Assess for malaria.
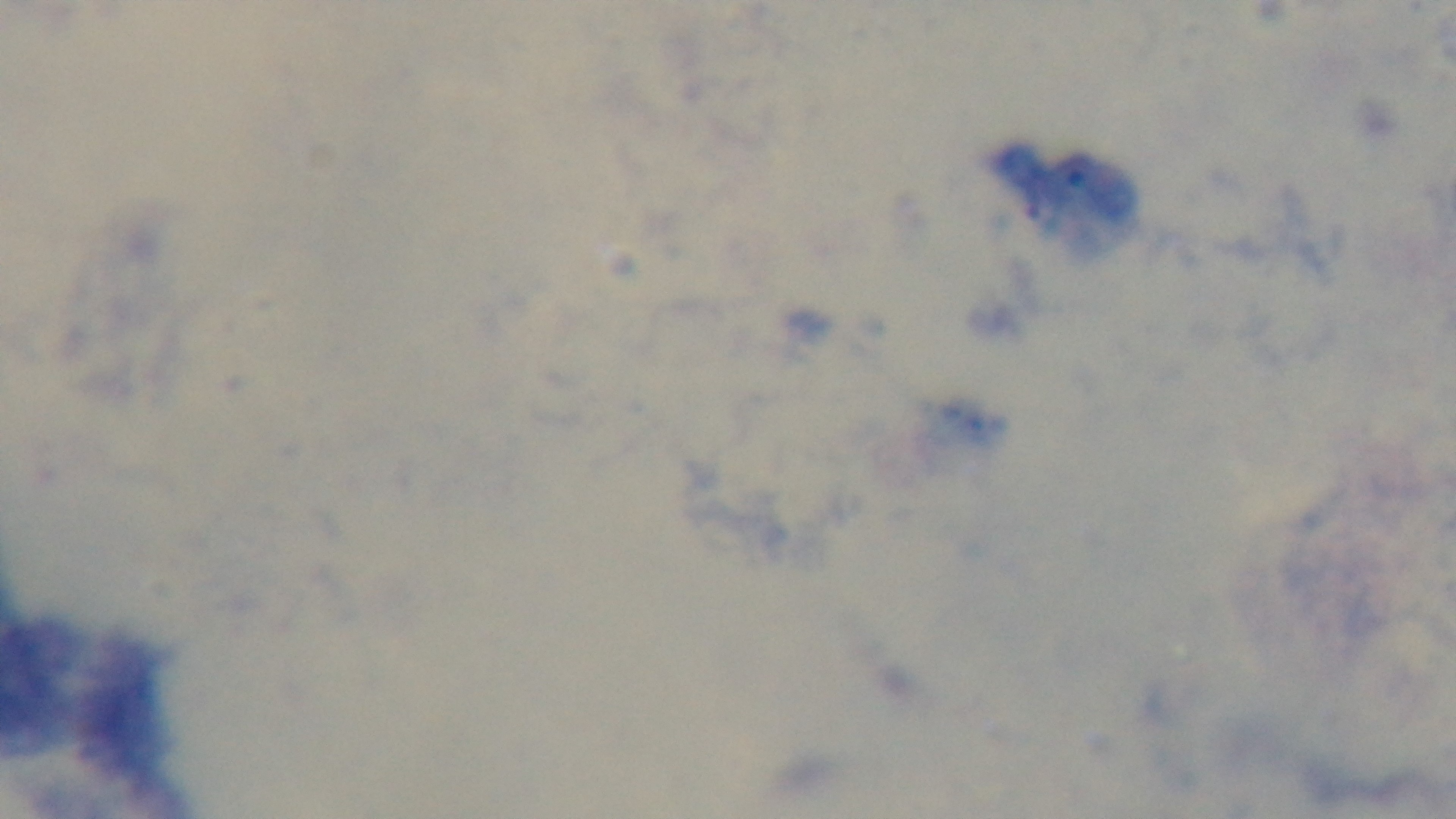
Negative.

preparation = thick smear
objective = 100x oil immersion
modality = light microscopy
field of view = single
stain = Giemsa
capture = mounted 4K digital camera